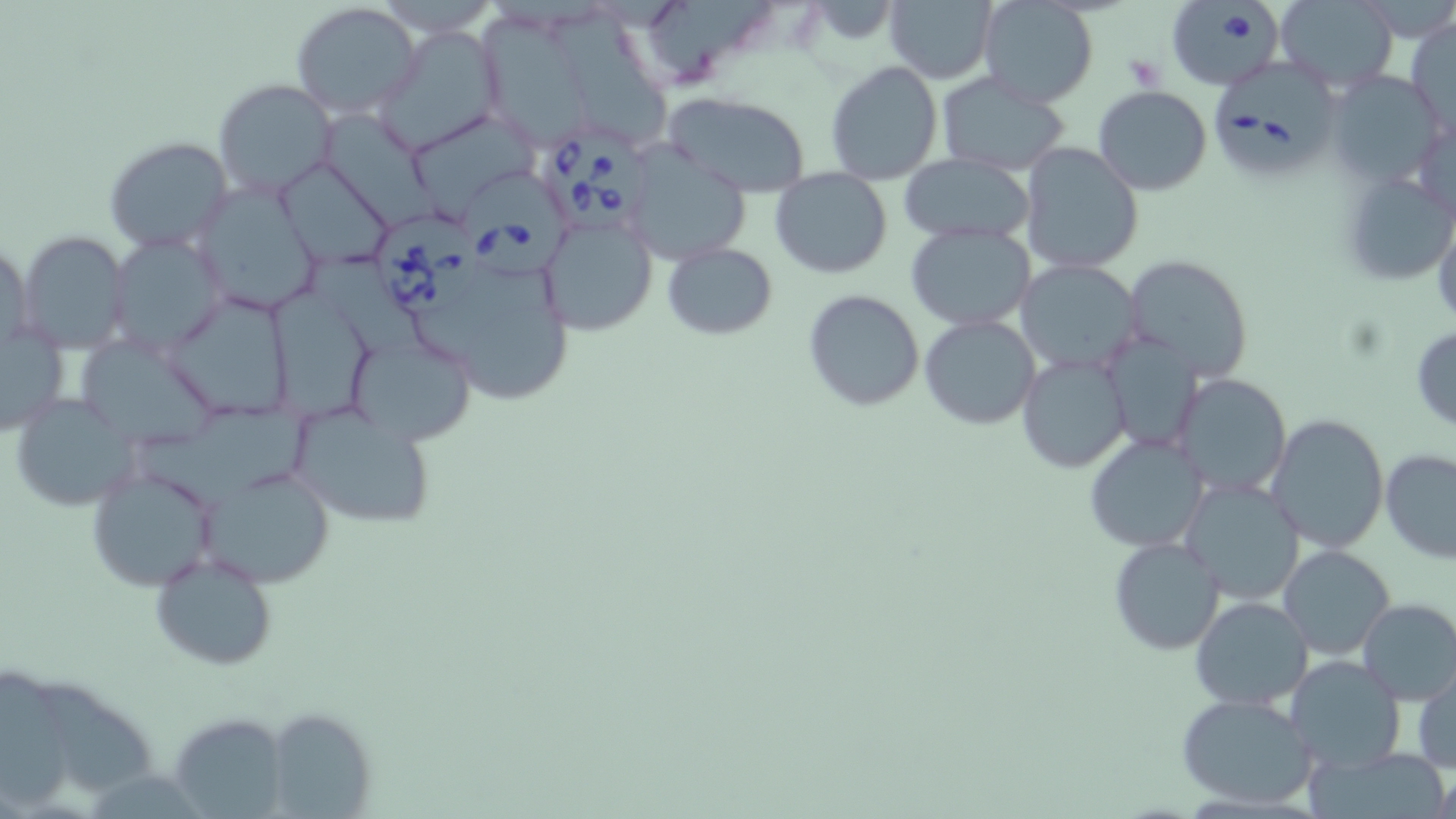

Approximate bounding boxes as (x1,y1)-(x2,y2) corner pairs in pixels. Uninfected red blood cell locations: (883,0)-(998,85), (979,0)-(1100,108), (1275,0)-(1398,92), (290,1)-(424,119), (1406,13)-(1455,132), (551,17)-(670,148), (484,18)-(584,149), (375,26)-(505,154), (825,61)-(943,185), (1328,71)-(1446,189), (935,72)-(1072,175), (213,79)-(339,198), (1093,85)-(1212,197), (663,89)-(812,198), (321,112)-(443,232), (415,115)-(541,216), (103,135)-(233,253), (623,142)-(750,265), (1019,143)-(1145,273), (900,154)-(1035,245), (276,158)-(396,270), (1339,166)-(1456,286), (770,168)-(892,278), (191,179)-(325,315), (539,215)-(658,337), (906,223)-(1035,330), (17,229)-(133,351), (110,232)-(228,354), (2,238)-(35,352), (663,243)-(778,340), (409,244)-(578,405), (1123,254)-(1253,382), (1138,256)-(1270,497), (1016,260)-(1143,375), (271,285)-(372,424), (803,289)-(925,411), (167,292)-(291,424), (919,314)-(1041,430), (0,326)-(68,436), (1410,326)-(1456,432), (356,331)-(471,445), (1102,333)-(1204,455), (75,335)-(226,452), (1017,354)-(1131,473), (1171,373)-(1292,498), (9,394)-(141,511), (140,404)-(319,511), (290,408)-(439,530), (1267,413)-(1389,554), (1083,434)-(1208,553), (1379,449)-(1456,562), (85,465)-(221,592), (201,466)-(337,588), (1182,480)-(1305,603), (1108,537)-(1225,656), (1279,544)-(1395,659), (149,552)-(278,672), (1190,596)-(1312,710), (1354,598)-(1456,704), (1284,655)-(1407,773), (1413,661)-(1455,776), (1,670)-(70,808), (37,681)-(153,796), (1174,692)-(1319,811), (261,707)-(376,818), (169,712)-(289,817). Platelet locations: (1125,53)-(1163,90). Babesia divergens-infected red blood cell locations: (1166,2)-(1285,90), (1212,62)-(1343,180), (544,130)-(658,236), (457,169)-(570,280), (374,216)-(483,314). Slide-level diagnosis: Babesia divergens. Optical microscopy. Single field of view. Image is 1456×819 pixels. Thin blood film. Captured at 1000x magnification. May-Grünwald-Giemsa stain.